Assess for Plasmodium parasites.
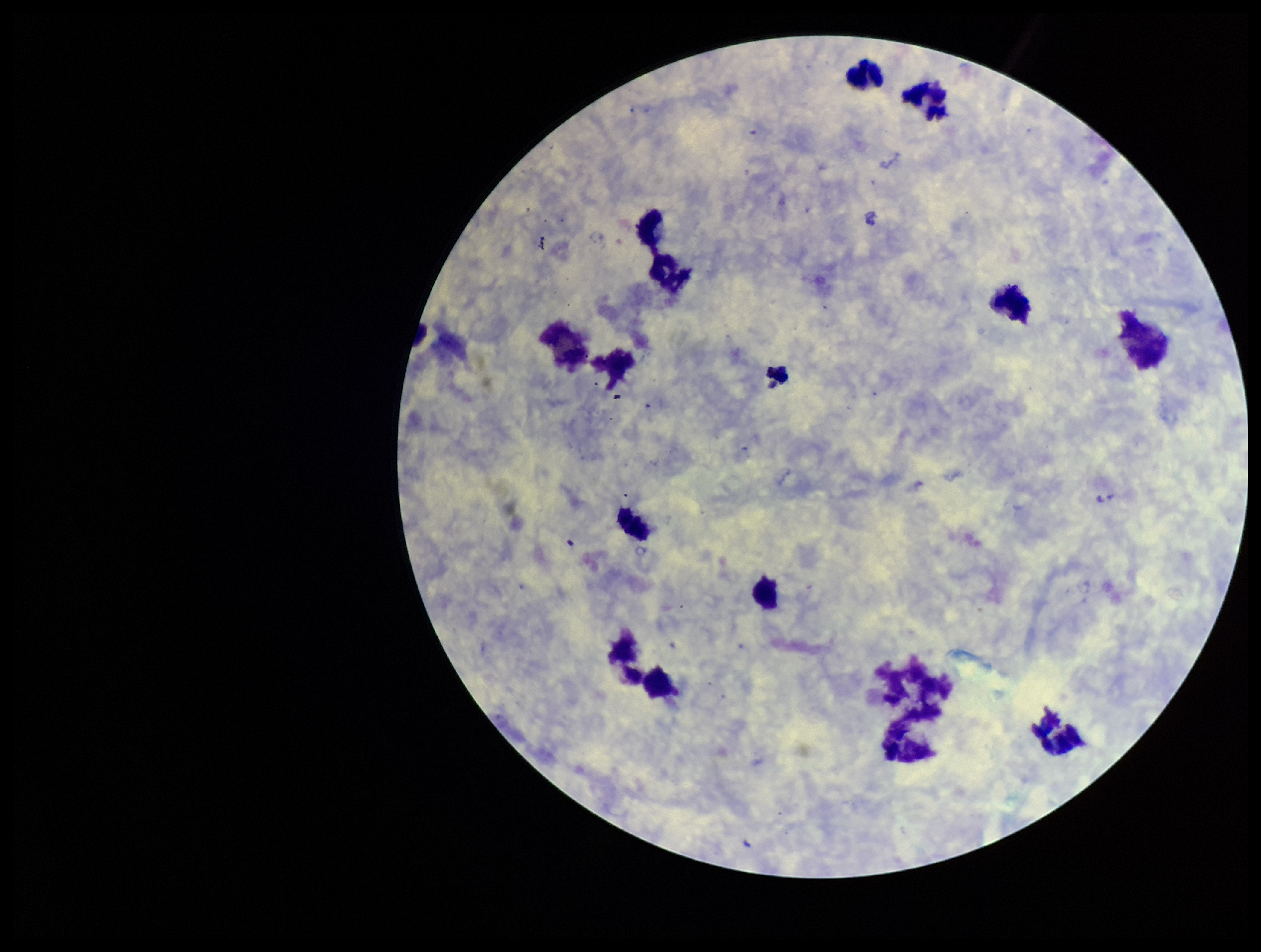

None detected.

Summary:
  - Preparation: thick
  - Capture: smartphone photograph through the microscope eyepiece
  - Parasite count: 0
  - Leukocyte count: 14
  - Stain: Giemsa
  - Patient malaria status: negative
  - Image size: 1261×952 pixels
  - Field of view: one from this slide